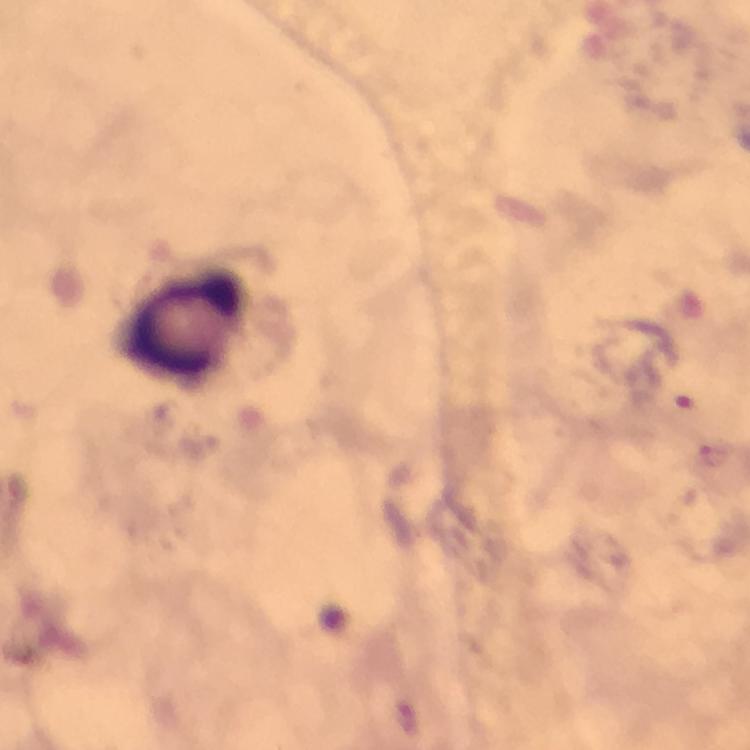

context: from a diagnostic examination for malaria
preparation: thick blood film
capture: smartphone mounted on the microscope
magnification: 100x
image_size: 750×750 pixels
leukocyte_locations: 'approximate centers as {x, y} in pixels: {182, 322}'
cropped_from: a single field of view
stain: Giemsa
malaria_parasite_locations: 'approximate centers as {x, y} in pixels: {715, 455}, {403, 716}'
immersion_oil: used